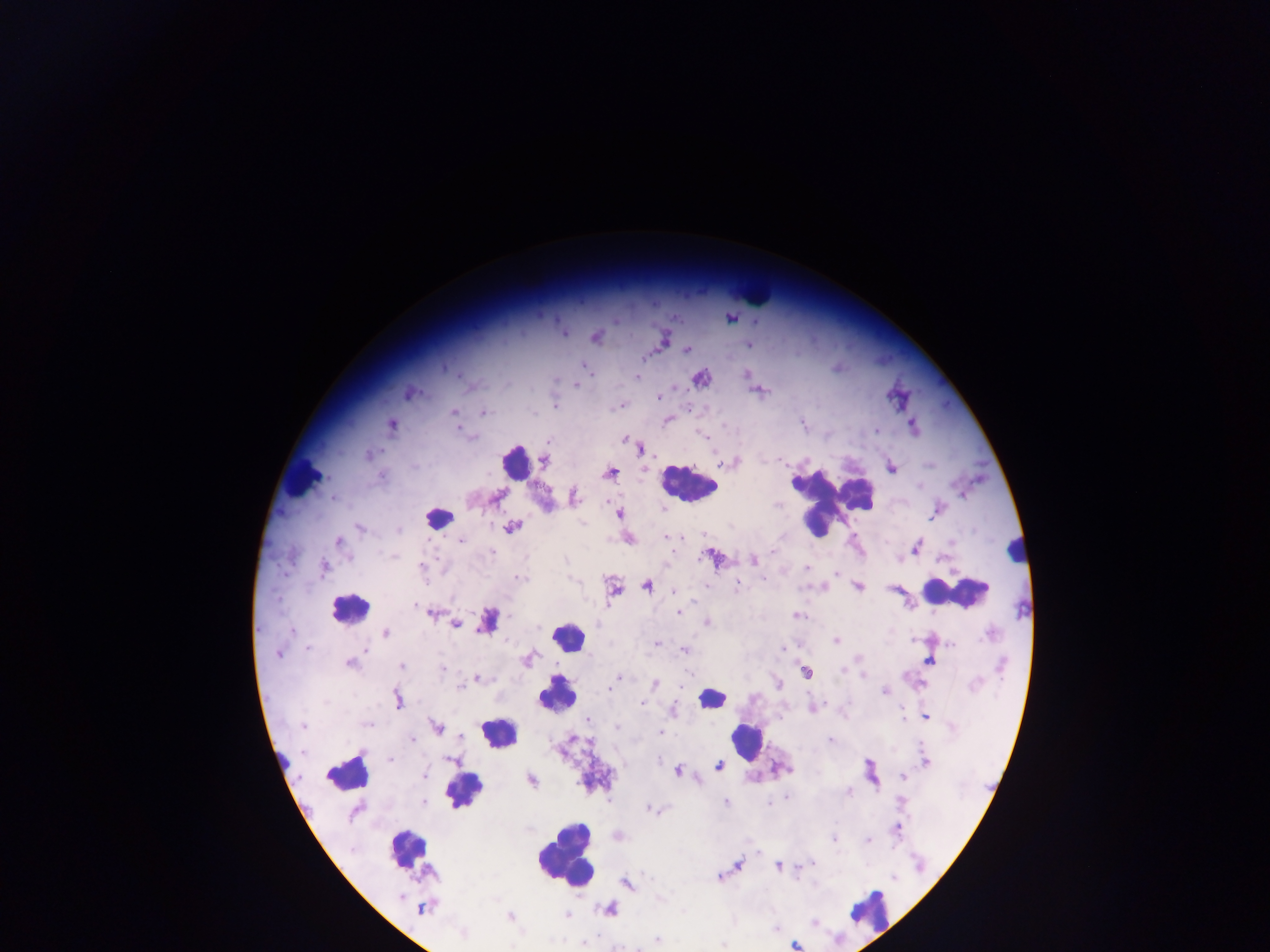

leukocyte locations = approximate centers as x y in pixels: 756 292; 514 462; 302 480; 689 483; 832 498; 439 517; 1016 550; 956 591; 349 608; 567 638; 557 692; 712 697; 496 733; 747 740; 347 772; 464 789; 407 849; 566 850; 867 910
capture = mobile-phone photograph through a microscope
image size = 1270×952 pixels
preparation = thick blood film
Plasmodium parasite locations = approximate centers as x y in pixels: 731 313; 674 317; 731 318; 614 320; 756 321; 563 333; 595 337; 663 340; 749 344; 686 350; 583 365; 587 370; 746 375; 637 377; 700 377; 576 384; 757 391; 409 393; 657 396; 898 398; 620 405; 554 406; 453 411; 482 412; 666 420; 391 424; 458 427; 913 427; 876 431; 624 438; 547 442; 638 446; 369 455; 544 459; 728 462; 891 468; 609 472; 495 497; 573 497; 937 510; 619 513; 512 527; 360 528; 665 536; 627 538; 460 540; 338 542; 916 547; 713 557; 753 559; 421 566; 324 567; 805 568; 837 573; 517 578; 737 583; 646 585; 857 586; 612 587; 895 589; 673 590; 430 612; 679 612; 797 615; 487 621; 707 622; 456 625; 385 633; 837 640; 655 644; 951 645; 307 646; 782 646; 685 650; 278 653; 528 659; 928 660; 350 663; 401 665; 442 669; 806 671; 618 677; 476 678; 615 681; 777 683; 654 684; 884 691; 397 699; 640 703; 812 708; 672 710; 925 717; 587 719; 303 725; 436 727; 662 733; 412 740; 829 740; 390 758; 452 760; 925 761; 719 766; 676 771; 423 774; 903 776; 530 779; 847 791; 787 797; 726 803; 651 809; 898 827; 618 836; 834 838; 868 840; 757 853; 736 865; 778 866; 799 867; 718 877; 627 883; 423 907; 609 908; 566 915; 510 917; 815 922; 462 934; 656 939; 583 942; 723 944; 794 944
country = Ghana
field of view = single